Assess this cell for malaria.
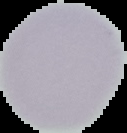
Uninfected.

preparation: thin blood smear
image_size: 127×133 pixels
image_type: cell region segmented out of the field of view; surrounding area masked to black